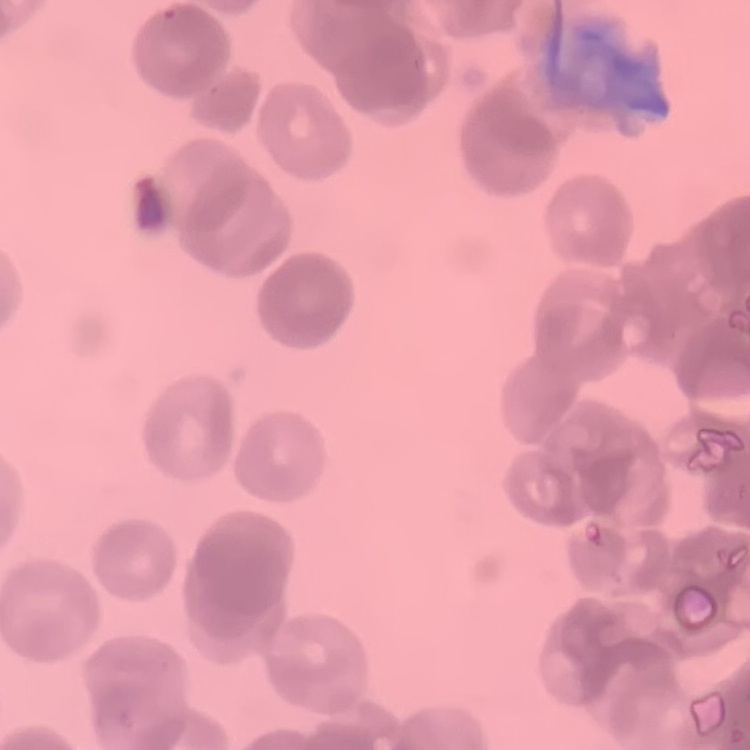 The erythrocytes show rouleaux formation. Thin blood smear. Stained with either Field's or Giemsa. One tile cut from a larger photomicrograph.